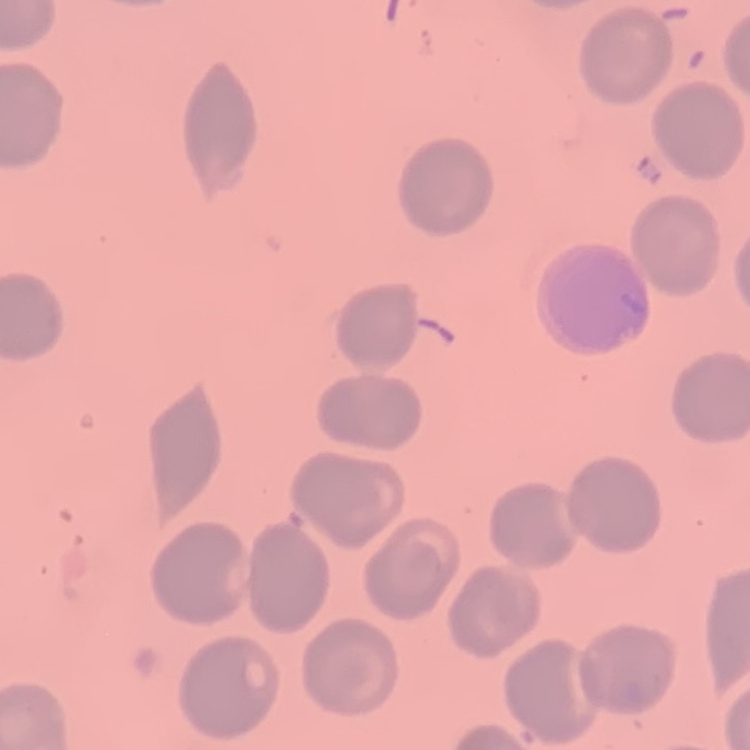

erythrocyte_morphology: no rouleaux formation
preparation: thin blood film
image_type: one tile cut from a larger photomicrograph
stain: Field's or Giemsa